Locate every uninfected red blood cell.
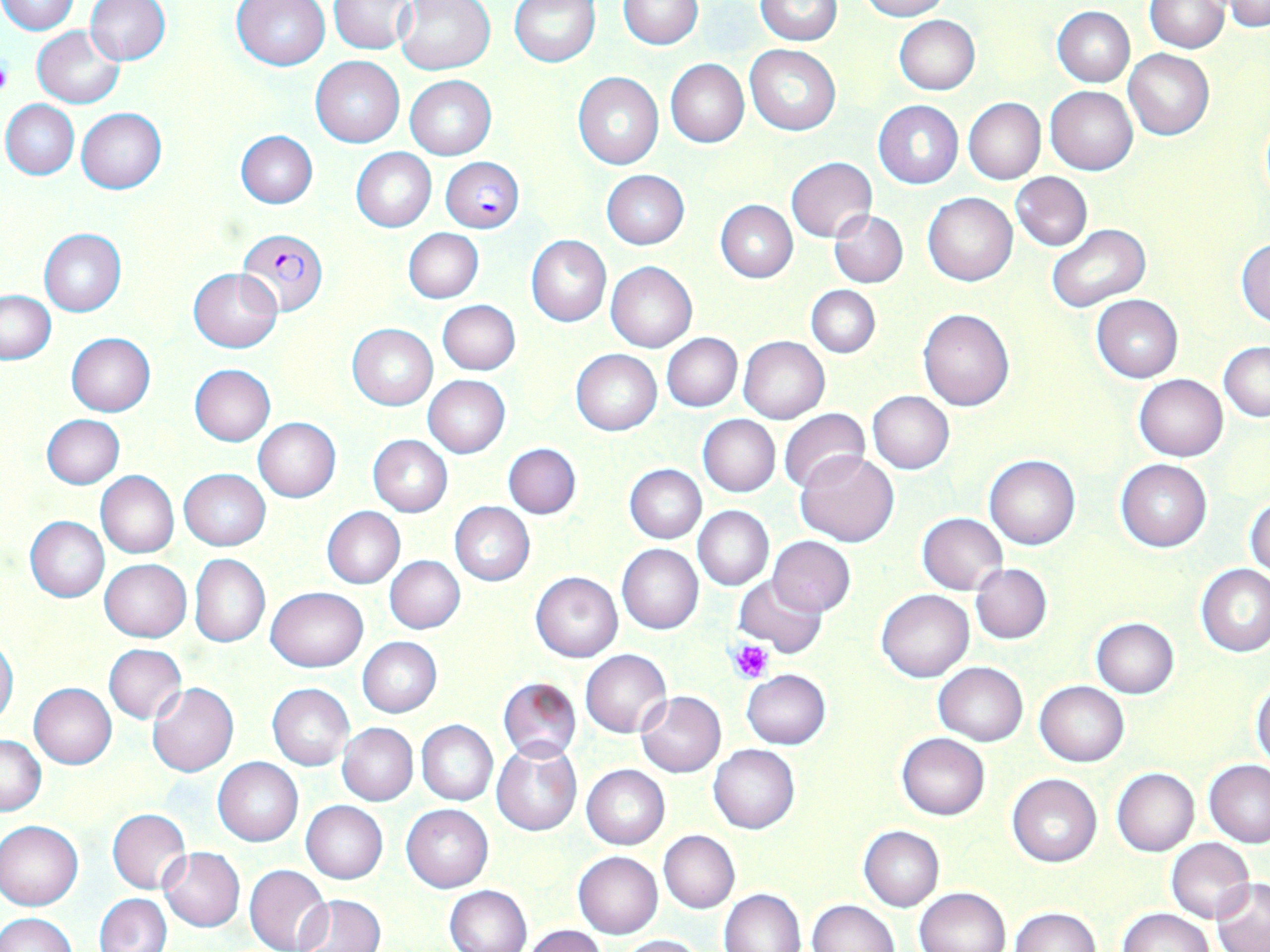

Approximate bounding boxes as [x1, y1, x2, y2] in pixels.
Uninfected red blood cells: [0, 0, 80, 34], [84, 0, 170, 65], [330, 0, 415, 53], [394, 0, 495, 75], [510, 0, 601, 66], [755, 0, 843, 45], [856, 0, 949, 20], [1146, 0, 1227, 52], [1226, 0, 1269, 32], [232, 1, 331, 69], [617, 1, 703, 50], [1053, 6, 1134, 87], [893, 15, 980, 95], [32, 26, 124, 107], [744, 45, 840, 136], [1123, 49, 1214, 140], [309, 55, 405, 148], [665, 58, 749, 147], [573, 73, 664, 170], [406, 76, 495, 159], [1045, 85, 1138, 175], [963, 97, 1045, 183], [2, 99, 79, 179], [874, 101, 962, 188], [77, 108, 166, 194], [236, 130, 317, 208], [351, 149, 436, 231], [785, 156, 877, 242], [601, 170, 690, 250], [1012, 172, 1091, 250], [923, 192, 1017, 286], [715, 200, 797, 283], [830, 211, 907, 287], [1046, 224, 1150, 312], [38, 229, 125, 317], [403, 229, 483, 303], [526, 235, 610, 326], [1236, 238, 1270, 326], [605, 262, 698, 352], [189, 268, 281, 353], [806, 286, 880, 358], [2, 290, 55, 364], [1091, 295, 1182, 382], [438, 300, 520, 375], [917, 308, 1015, 411], [348, 324, 437, 409], [65, 333, 157, 416], [662, 333, 742, 411], [738, 337, 828, 424], [1219, 342, 1270, 421], [571, 349, 662, 435], [190, 364, 275, 446], [1133, 373, 1228, 461], [423, 376, 510, 457], [867, 390, 954, 475], [778, 408, 871, 494], [42, 414, 124, 489], [698, 414, 781, 497], [253, 418, 341, 502], [368, 434, 452, 516], [504, 443, 581, 519], [796, 450, 899, 547], [985, 455, 1080, 550], [1115, 459, 1211, 551], [624, 464, 705, 543], [179, 469, 270, 551], [96, 471, 179, 558], [1247, 494, 1269, 579], [450, 502, 535, 585], [693, 505, 773, 590], [322, 506, 404, 589], [918, 513, 1007, 595], [25, 517, 109, 602], [768, 536, 856, 615], [617, 544, 704, 634], [190, 555, 270, 647], [385, 556, 465, 633], [100, 559, 191, 641], [970, 563, 1052, 645], [1196, 564, 1270, 656], [530, 571, 622, 662], [735, 574, 827, 659], [266, 587, 368, 672], [877, 590, 972, 683], [1090, 617, 1180, 698], [0, 637, 18, 728], [358, 637, 442, 717], [104, 644, 187, 725], [580, 650, 670, 737], [934, 661, 1027, 746], [741, 669, 830, 749], [498, 677, 581, 762], [1035, 681, 1129, 766], [148, 682, 239, 776], [1252, 682, 1270, 767], [28, 683, 117, 768], [267, 683, 355, 770], [636, 690, 726, 777], [417, 720, 497, 806], [337, 723, 417, 806], [896, 732, 989, 820], [0, 733, 46, 816], [491, 741, 582, 836], [708, 744, 800, 834], [213, 757, 302, 846], [1204, 760, 1270, 847], [580, 764, 669, 849], [1111, 768, 1199, 856], [1007, 773, 1101, 867], [301, 800, 388, 883], [402, 804, 493, 892], [106, 809, 190, 893], [0, 819, 84, 910], [858, 826, 944, 911], [659, 830, 739, 913], [1166, 837, 1256, 923], [159, 847, 245, 931], [572, 851, 663, 938], [245, 864, 333, 952], [1210, 880, 1270, 951], [445, 885, 531, 952], [915, 886, 1012, 952], [719, 888, 806, 952], [95, 893, 171, 952], [294, 895, 385, 951], [808, 899, 898, 951], [1009, 907, 1100, 952], [1118, 909, 1217, 952], [0, 912, 76, 952], [523, 925, 608, 952], [613, 934, 706, 952].

Summary:
  - Plasmodium falciparum-infected red blood cell locations: [442, 157, 525, 234], [237, 229, 328, 318]
  - Platelet locations: [0, 54, 14, 100], [731, 639, 774, 682]
  - Slide-level diagnosis: Plasmodium falciparum
  - Field of view: one of a larger specimen
  - Stain: May-Grünwald-Giemsa
  - Preparation: thin blood smear
  - Modality: optical microscopy
  - Magnification: 1000x
  - Image size: 1270×952 pixels